Assess this cell for malaria.
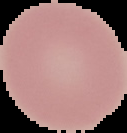

Uninfected.

Summary:
  - Image size: 127×133 pixels
  - Preparation: thin blood smear
  - Image type: cell region segmented out of the field of view; surrounding area masked to black